Describe the morphology of the red blood cells.
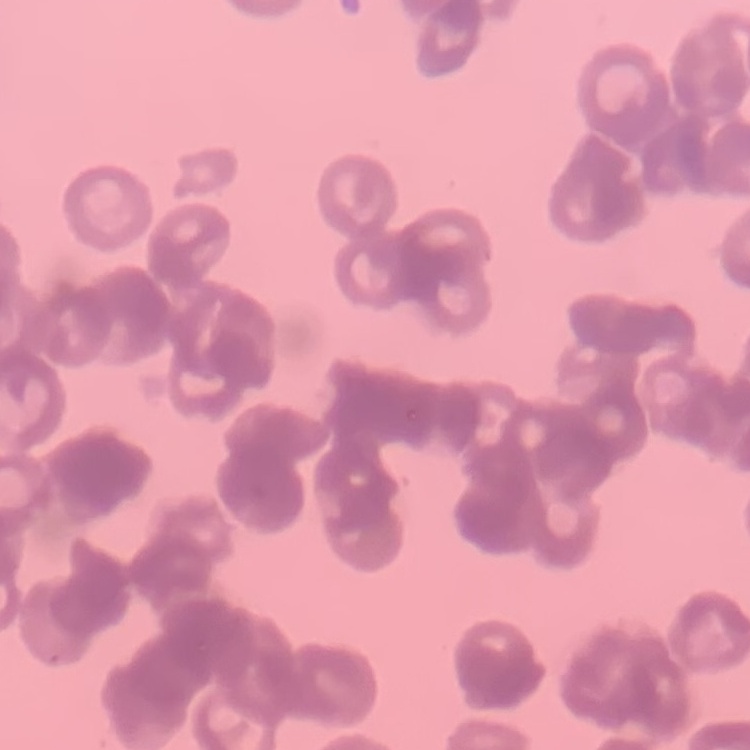

Rouleaux formation.

Summary:
  - Preparation: thin blood smear
  - Stain: Field's or Giemsa
  - Image type: square crop of a larger photomicrograph